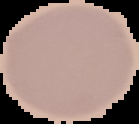
Summary:
  - Malaria status: uninfected
  - Image type: segmented cell region with the area outside set to black
  - Preparation: thin blood smear
  - Image size: 139×124 pixels